Name the parasite shown.
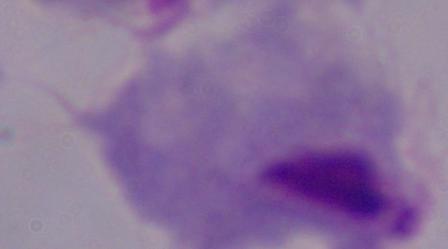

This is a trichomonad.

Summary:
  - Modality: photomicrograph
  - Magnification: 1000x